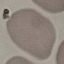
Summary:
  - Result: no malaria parasites seen
  - Stain: Giemsa
  - Image type: automatically extracted cell patch, resized to 64 × 64 pixels
  - Preparation: thin blood smear
  - Capture: smartphone camera at the microscope eyepiece